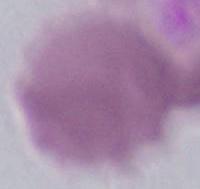
An erythrocyte is shown. Photomicrograph. Captured at 1000x magnification.